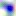
modality: photomicrograph
magnification: 400x
identification: Toxoplasma gondii